Report the malaria status of this cell.
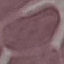

It is uninfected.

Giemsa stain. Automatically extracted cell patch, resized to 64 × 64 pixels. Photographed with a smartphone camera at the microscope eyepiece. Thin smear of blood.